Report the malaria status of this cell.
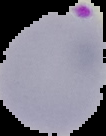

It is parasitized.

Segmented cell region on a black background. From a thin blood film. Image is 106×136 pixels.